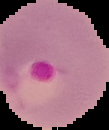

{
  "image_type": "segmented cell region with the area outside set to black",
  "preparation": "thin blood film",
  "image_size": "109×130 pixels",
  "malaria_status": "parasitized"
}